Report the malaria status of this cell.
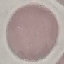
It is uninfected.

preparation = thin blood film
capture = smartphone through the microscope eyepiece
image type = cell patch, automatically extracted from a larger field of view and resized to 64 × 64 pixels
stain = Giemsa